Assess this cell for malaria.
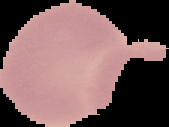
Uninfected.

Summary:
  - Preparation: thin blood smear
  - Image type: segmented cell region on a black background
  - Image size: 169×127 pixels